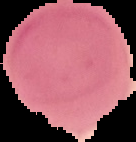
Malaria status: uninfected. From a thin blood smear. Image is 136×142 pixels. Cell region segmented out of the field of view; the surrounding area is masked to black.